Assess the morphology of the erythrocytes.
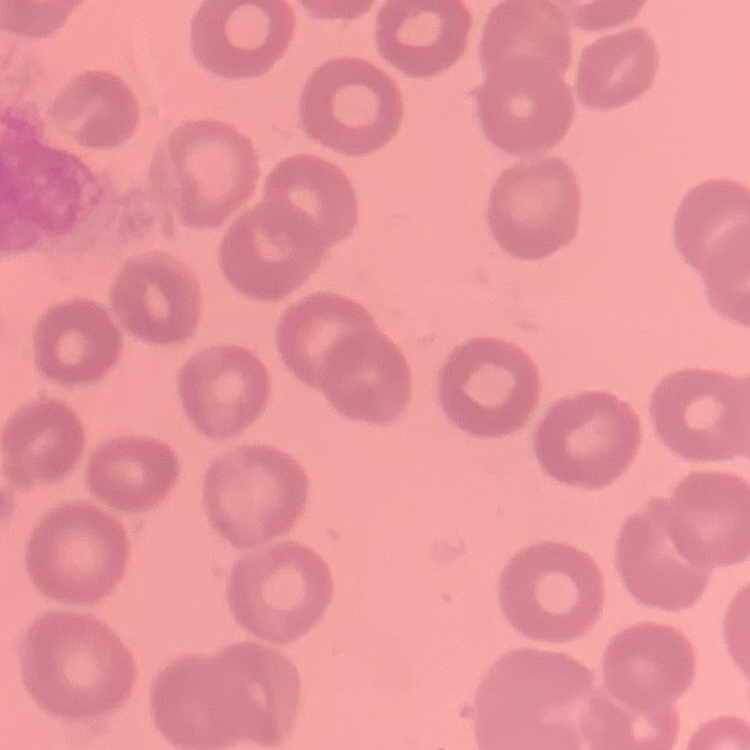
They show no rouleaux formation.

preparation = thin peripheral smear
image type = square crop of a larger photomicrograph
stain = Field's or Giemsa